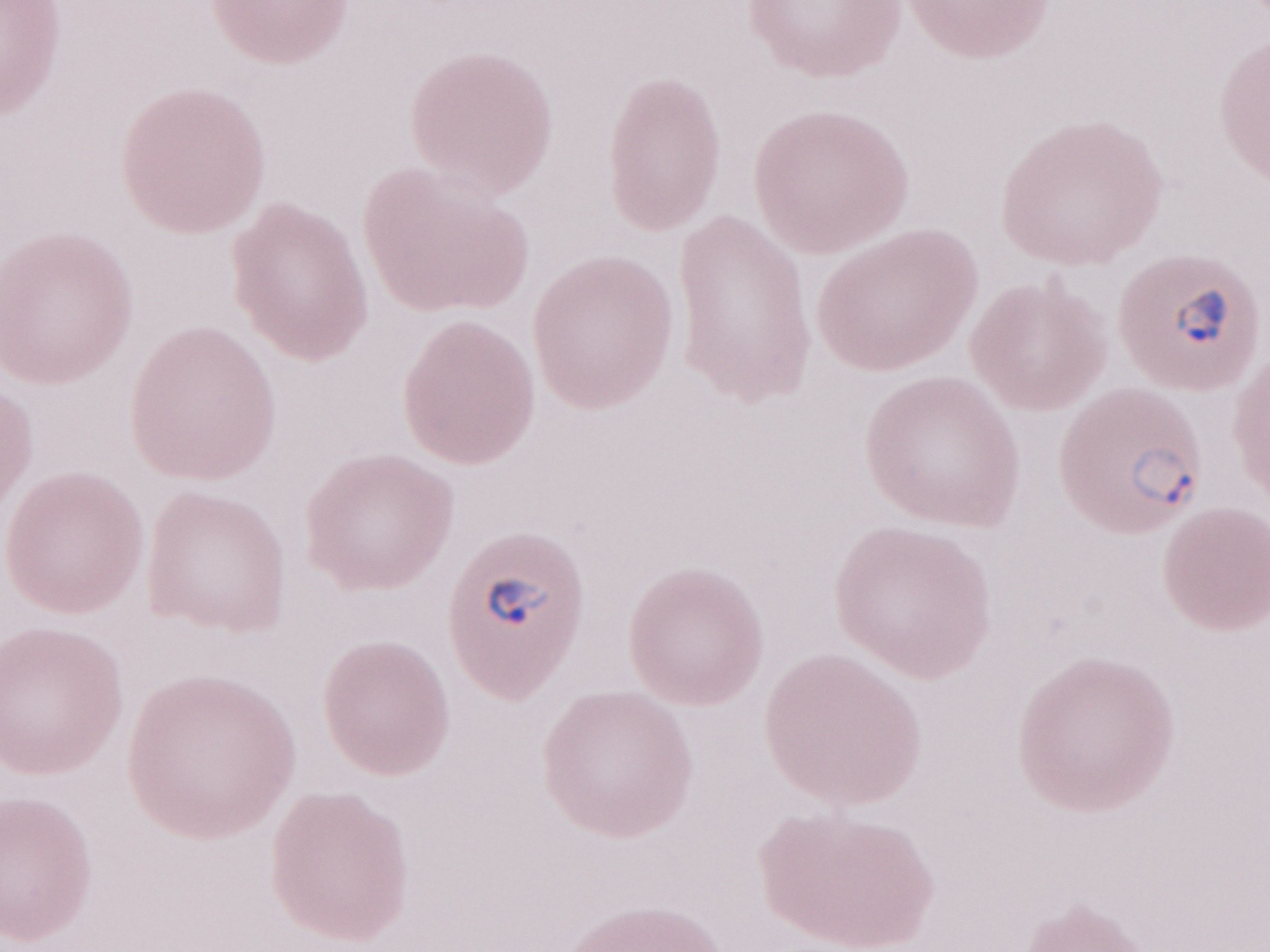 Thin peripheral-blood smear. May-Grünwald-Giemsa stain. Magnification: 1,000x. Image is 1270×952 pixels. One field of this slide. Patient-level malaria diagnosis: positive. Olympus BX43 microscope and DP73 digital camera.